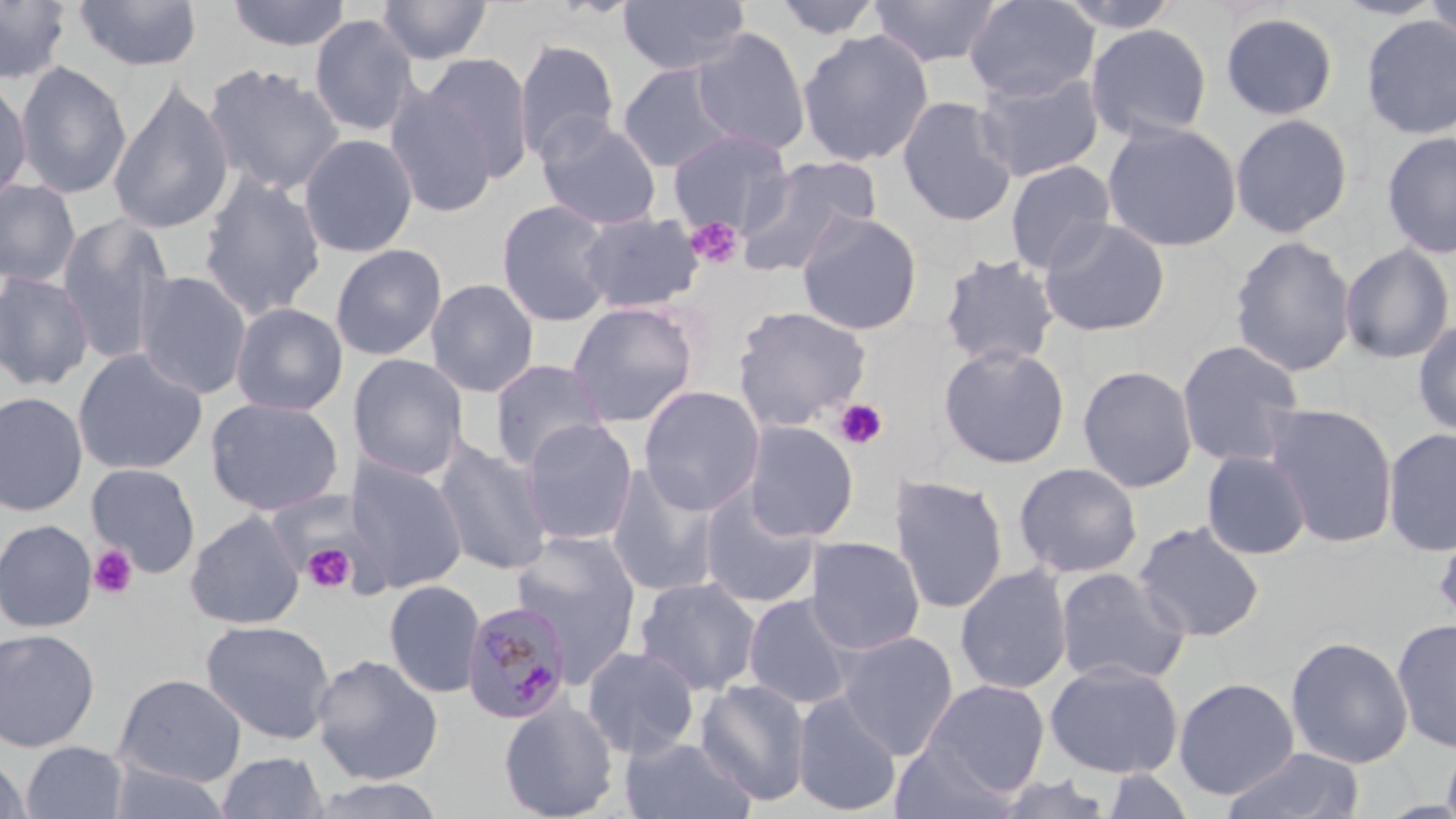

Approximate bounding boxes as [x1, y1, x2, y2] in pixels. Uninfected red blood cell locations: [73, 0, 202, 73], [227, 0, 352, 53], [376, 0, 492, 66], [617, 0, 750, 77], [772, 0, 885, 41], [964, 0, 1099, 102], [1052, 0, 1184, 32], [1421, 0, 1456, 54], [0, 1, 72, 86], [867, 1, 1002, 69], [1220, 12, 1339, 121], [309, 14, 419, 139], [1360, 15, 1456, 140], [1085, 23, 1213, 143], [691, 27, 811, 156], [797, 29, 934, 167], [514, 38, 620, 164], [423, 51, 536, 182], [15, 61, 131, 200], [203, 62, 345, 196], [617, 62, 741, 173], [973, 69, 1105, 182], [0, 77, 32, 208], [108, 79, 234, 236], [383, 82, 498, 219], [896, 95, 1018, 227], [1230, 113, 1354, 238], [536, 115, 663, 231], [1101, 119, 1243, 252], [667, 129, 793, 235], [1381, 131, 1456, 259], [299, 134, 418, 258], [734, 155, 881, 277], [1004, 160, 1117, 275], [198, 173, 327, 320], [0, 179, 81, 288], [496, 199, 617, 327], [577, 211, 705, 314], [796, 212, 923, 336], [55, 214, 174, 366], [1037, 218, 1171, 337], [1229, 234, 1356, 376], [329, 243, 447, 361], [1339, 243, 1455, 364], [938, 253, 1061, 369], [0, 271, 95, 391], [135, 271, 252, 399], [425, 278, 540, 397], [566, 300, 700, 428], [230, 302, 348, 416], [731, 305, 873, 432], [1412, 319, 1456, 439], [1176, 340, 1307, 468], [937, 343, 1071, 469], [72, 348, 208, 475], [347, 353, 469, 480], [488, 360, 611, 472], [1077, 365, 1198, 492], [638, 385, 765, 515], [0, 391, 88, 517], [204, 397, 345, 516], [1263, 403, 1399, 547], [518, 418, 639, 546], [741, 420, 859, 542], [1382, 427, 1456, 556], [433, 439, 554, 576], [1201, 451, 1312, 560], [345, 457, 468, 594], [605, 462, 724, 599], [1014, 462, 1143, 579], [85, 463, 201, 577], [890, 475, 1009, 615], [698, 486, 822, 609], [185, 511, 304, 630], [0, 519, 97, 632], [1433, 520, 1456, 633], [1133, 521, 1266, 642], [509, 530, 643, 680], [804, 537, 926, 654], [954, 565, 1074, 695], [1054, 566, 1191, 688], [634, 577, 763, 697], [383, 579, 485, 698], [742, 592, 860, 710], [1392, 617, 1456, 754], [200, 619, 336, 745], [0, 627, 101, 752], [836, 631, 959, 759], [1285, 635, 1413, 768], [581, 646, 701, 759], [310, 653, 444, 785], [1045, 660, 1184, 778], [113, 673, 247, 787], [694, 677, 812, 806], [1173, 677, 1300, 799], [925, 679, 1050, 794], [792, 691, 902, 816], [498, 699, 619, 819], [621, 735, 757, 819], [1440, 735, 1456, 819], [891, 739, 1020, 819], [21, 741, 129, 819], [1220, 745, 1368, 819], [215, 751, 330, 819], [0, 752, 33, 819], [104, 760, 234, 819], [1099, 767, 1198, 819], [988, 772, 1117, 818], [302, 775, 448, 819]. Platelet locations: [685, 216, 744, 268], [833, 398, 888, 448], [88, 544, 137, 599], [301, 544, 356, 594]. Plasmodium malariae-infected red blood cell locations: [461, 600, 573, 726]. Slide-level diagnosis: Plasmodium malariae. Image is 1456×819 pixels. Captured at 1000x magnification. Single field of view. Optical microscopy. May-Grünwald-Giemsa stain. Thin blood smear.